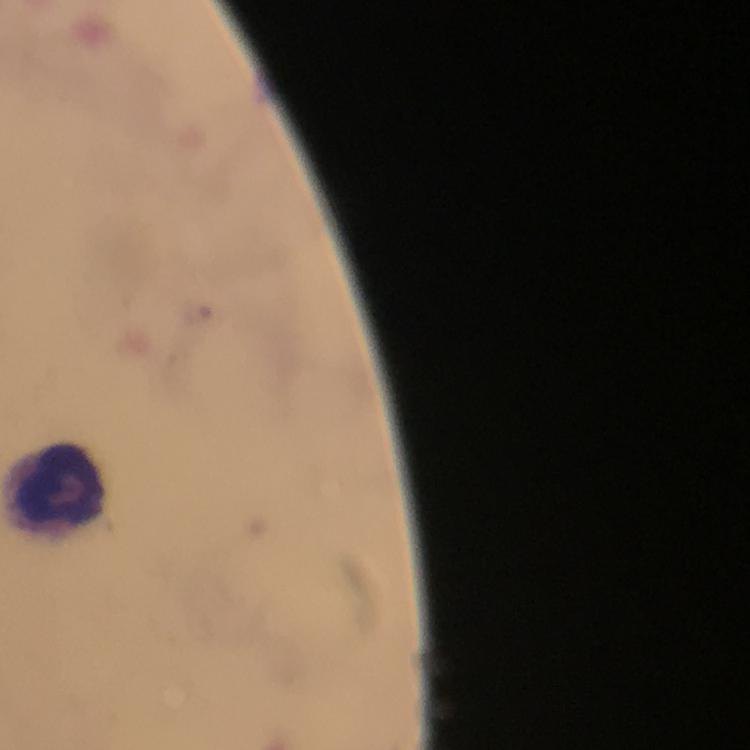

Approximate object centers, in pixels from the top-left corner.
Summary:
  - Leukocyte locations: (x=60, y=486)
  - Immersion oil: used
  - Magnification: 100x
  - Preparation: thick smear
  - Cropped from: one field of view
  - Stain: Giemsa
  - Image size: 750×750 pixels
  - Context: from a malaria diagnostic workup
  - Plasmodium parasites: none seen
  - Capture: smartphone mounted on the microscope